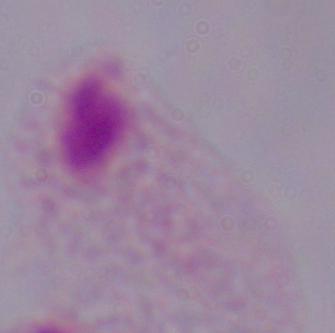
1000x magnification. Photomicrograph. A trichomonad is seen.